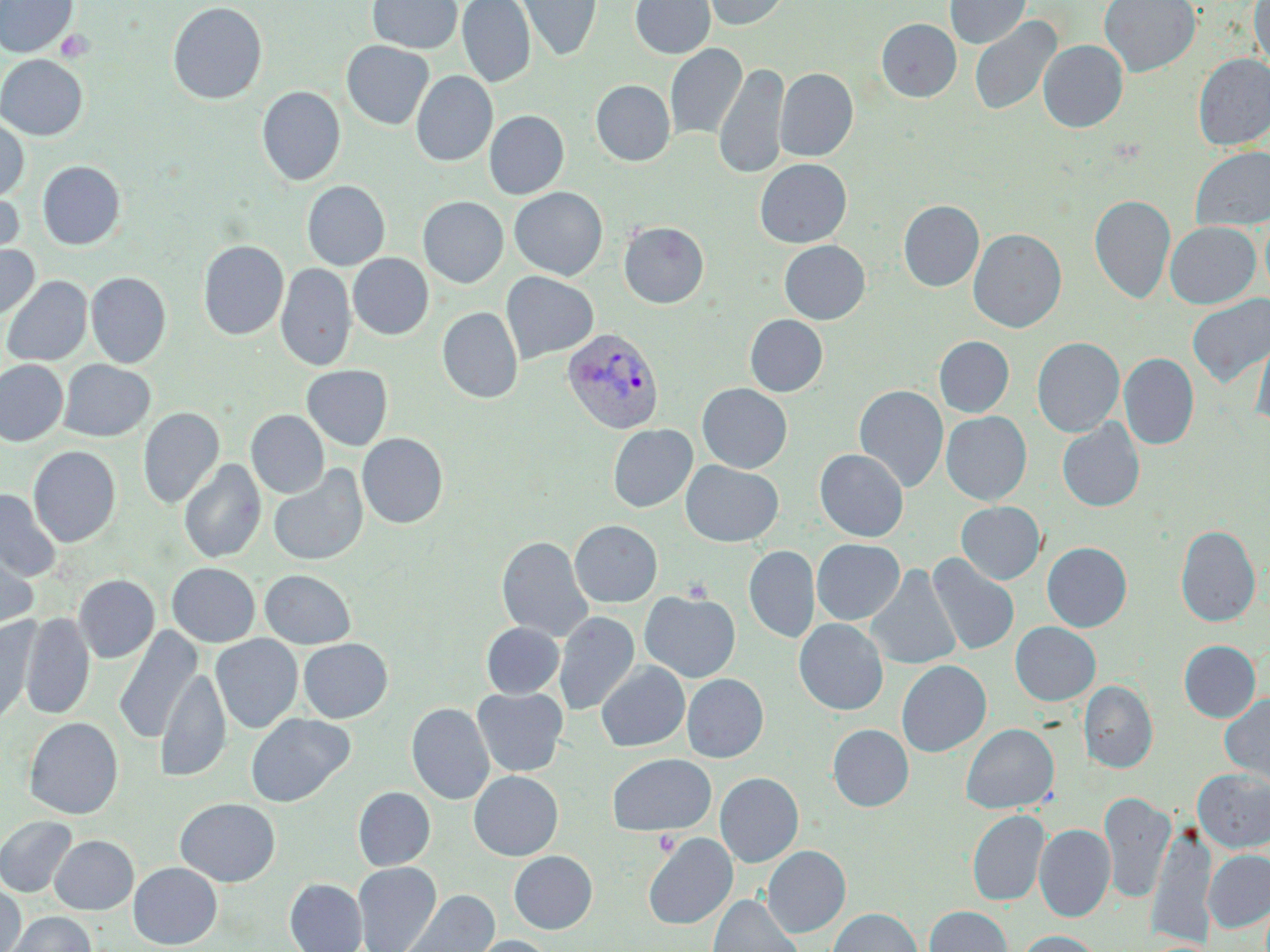

Approximate bounding boxes as named x1/y1/x2/y2 corners in pixels. Platelet locations: (x1=56, y1=30, x2=95, y2=62), (x1=681, y1=576, x2=714, y2=602), (x1=653, y1=830, x2=681, y2=856). Plasmodium vivax-infected red blood cell locations: (x1=561, y1=326, x2=666, y2=434). Uninfected red blood cell locations: (x1=0, y1=0, x2=78, y2=58), (x1=367, y1=0, x2=463, y2=54), (x1=457, y1=0, x2=535, y2=87), (x1=517, y1=0, x2=602, y2=62), (x1=630, y1=0, x2=715, y2=59), (x1=702, y1=0, x2=791, y2=30), (x1=946, y1=0, x2=1030, y2=49), (x1=1099, y1=0, x2=1200, y2=76), (x1=1249, y1=0, x2=1270, y2=68), (x1=167, y1=1, x2=267, y2=104), (x1=969, y1=16, x2=1062, y2=116), (x1=876, y1=19, x2=961, y2=102), (x1=53, y1=27, x2=96, y2=65), (x1=1038, y1=40, x2=1128, y2=132), (x1=342, y1=41, x2=434, y2=130), (x1=665, y1=43, x2=747, y2=141), (x1=1194, y1=53, x2=1270, y2=149), (x1=0, y1=54, x2=88, y2=140), (x1=714, y1=62, x2=789, y2=179), (x1=775, y1=67, x2=858, y2=162), (x1=411, y1=71, x2=497, y2=167), (x1=591, y1=80, x2=675, y2=166), (x1=257, y1=86, x2=346, y2=186), (x1=484, y1=110, x2=569, y2=199), (x1=0, y1=118, x2=30, y2=203), (x1=1191, y1=146, x2=1270, y2=230), (x1=754, y1=158, x2=852, y2=249), (x1=37, y1=161, x2=125, y2=249), (x1=302, y1=180, x2=390, y2=270), (x1=0, y1=187, x2=25, y2=265), (x1=509, y1=187, x2=608, y2=280), (x1=1090, y1=194, x2=1176, y2=304), (x1=418, y1=196, x2=508, y2=288), (x1=899, y1=200, x2=984, y2=292), (x1=618, y1=221, x2=709, y2=309), (x1=1165, y1=221, x2=1261, y2=308), (x1=968, y1=228, x2=1067, y2=333), (x1=198, y1=240, x2=288, y2=340), (x1=779, y1=240, x2=870, y2=324), (x1=0, y1=242, x2=39, y2=320), (x1=348, y1=253, x2=433, y2=340), (x1=199, y1=254, x2=352, y2=362), (x1=276, y1=263, x2=356, y2=371), (x1=501, y1=271, x2=599, y2=363), (x1=86, y1=272, x2=171, y2=368), (x1=2, y1=276, x2=92, y2=366), (x1=1187, y1=294, x2=1270, y2=388), (x1=437, y1=307, x2=523, y2=403), (x1=744, y1=314, x2=828, y2=397), (x1=1251, y1=329, x2=1270, y2=428), (x1=934, y1=336, x2=1014, y2=417), (x1=1032, y1=337, x2=1124, y2=437), (x1=1119, y1=353, x2=1199, y2=450), (x1=0, y1=359, x2=68, y2=446), (x1=58, y1=360, x2=155, y2=441), (x1=301, y1=364, x2=393, y2=450), (x1=697, y1=383, x2=792, y2=473), (x1=854, y1=385, x2=948, y2=492), (x1=138, y1=407, x2=224, y2=509), (x1=246, y1=410, x2=329, y2=498), (x1=941, y1=411, x2=1032, y2=505), (x1=1057, y1=419, x2=1145, y2=512), (x1=608, y1=424, x2=698, y2=512), (x1=357, y1=432, x2=448, y2=528), (x1=28, y1=445, x2=121, y2=547), (x1=815, y1=448, x2=908, y2=541), (x1=179, y1=458, x2=266, y2=564), (x1=680, y1=460, x2=784, y2=547), (x1=268, y1=464, x2=369, y2=566), (x1=7, y1=469, x2=104, y2=572), (x1=1, y1=489, x2=62, y2=581), (x1=956, y1=501, x2=1045, y2=584), (x1=569, y1=520, x2=662, y2=607), (x1=1175, y1=524, x2=1260, y2=627), (x1=496, y1=536, x2=592, y2=642), (x1=811, y1=538, x2=904, y2=624), (x1=1042, y1=542, x2=1132, y2=632), (x1=744, y1=545, x2=819, y2=643), (x1=0, y1=547, x2=37, y2=632), (x1=927, y1=554, x2=1019, y2=656), (x1=167, y1=563, x2=260, y2=647), (x1=866, y1=564, x2=961, y2=670), (x1=260, y1=569, x2=356, y2=649), (x1=74, y1=575, x2=159, y2=663), (x1=640, y1=591, x2=740, y2=682), (x1=554, y1=611, x2=639, y2=715), (x1=20, y1=612, x2=95, y2=720), (x1=794, y1=618, x2=889, y2=715), (x1=0, y1=619, x2=36, y2=727), (x1=481, y1=622, x2=564, y2=698), (x1=1011, y1=622, x2=1100, y2=706), (x1=114, y1=625, x2=203, y2=744), (x1=210, y1=634, x2=303, y2=733), (x1=298, y1=638, x2=392, y2=723), (x1=1179, y1=640, x2=1261, y2=721), (x1=896, y1=660, x2=991, y2=756), (x1=597, y1=661, x2=690, y2=752), (x1=155, y1=668, x2=231, y2=781), (x1=682, y1=673, x2=768, y2=762), (x1=1079, y1=680, x2=1157, y2=773), (x1=472, y1=687, x2=567, y2=776), (x1=1220, y1=695, x2=1270, y2=786), (x1=407, y1=702, x2=494, y2=805), (x1=246, y1=713, x2=354, y2=807), (x1=24, y1=717, x2=123, y2=819), (x1=962, y1=723, x2=1059, y2=813), (x1=828, y1=724, x2=913, y2=811), (x1=608, y1=753, x2=716, y2=836), (x1=1193, y1=768, x2=1270, y2=853), (x1=469, y1=771, x2=563, y2=861), (x1=715, y1=772, x2=803, y2=867), (x1=353, y1=787, x2=435, y2=870), (x1=1100, y1=791, x2=1175, y2=904), (x1=175, y1=797, x2=281, y2=886), (x1=967, y1=809, x2=1050, y2=906), (x1=0, y1=816, x2=78, y2=897), (x1=1035, y1=824, x2=1115, y2=921), (x1=1147, y1=824, x2=1216, y2=948), (x1=643, y1=833, x2=737, y2=930), (x1=49, y1=835, x2=138, y2=914), (x1=762, y1=846, x2=850, y2=937), (x1=1203, y1=850, x2=1270, y2=933), (x1=509, y1=851, x2=597, y2=934), (x1=129, y1=862, x2=222, y2=949), (x1=353, y1=862, x2=441, y2=952), (x1=285, y1=878, x2=367, y2=952), (x1=0, y1=881, x2=25, y2=952), (x1=398, y1=889, x2=500, y2=952), (x1=707, y1=894, x2=803, y2=952), (x1=925, y1=905, x2=1012, y2=952), (x1=828, y1=907, x2=922, y2=952), (x1=6, y1=911, x2=95, y2=952), (x1=1018, y1=930, x2=1102, y2=952), (x1=465, y1=935, x2=555, y2=952). Slide-level diagnosis: Plasmodium vivax. Thin blood smear. Captured at 1000x magnification. May-Grünwald-Giemsa-stained preparation. Image is 1270×952 pixels. One field of a larger specimen. Light microscopy.